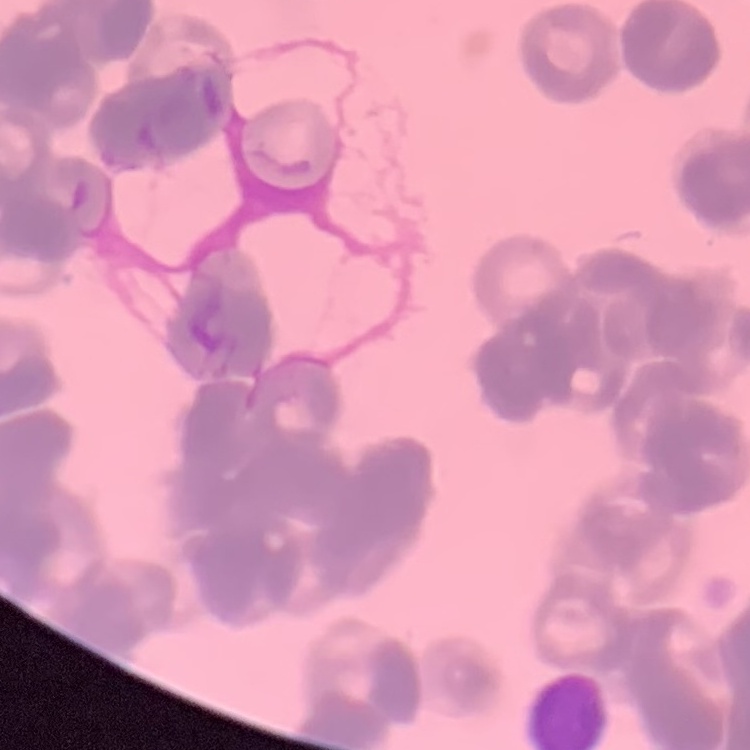
{
  "erythrocyte_morphology": "rouleaux formation",
  "stain": "Field's or Giemsa",
  "preparation": "thin blood smear",
  "image_type": "square crop of a larger photomicrograph"
}